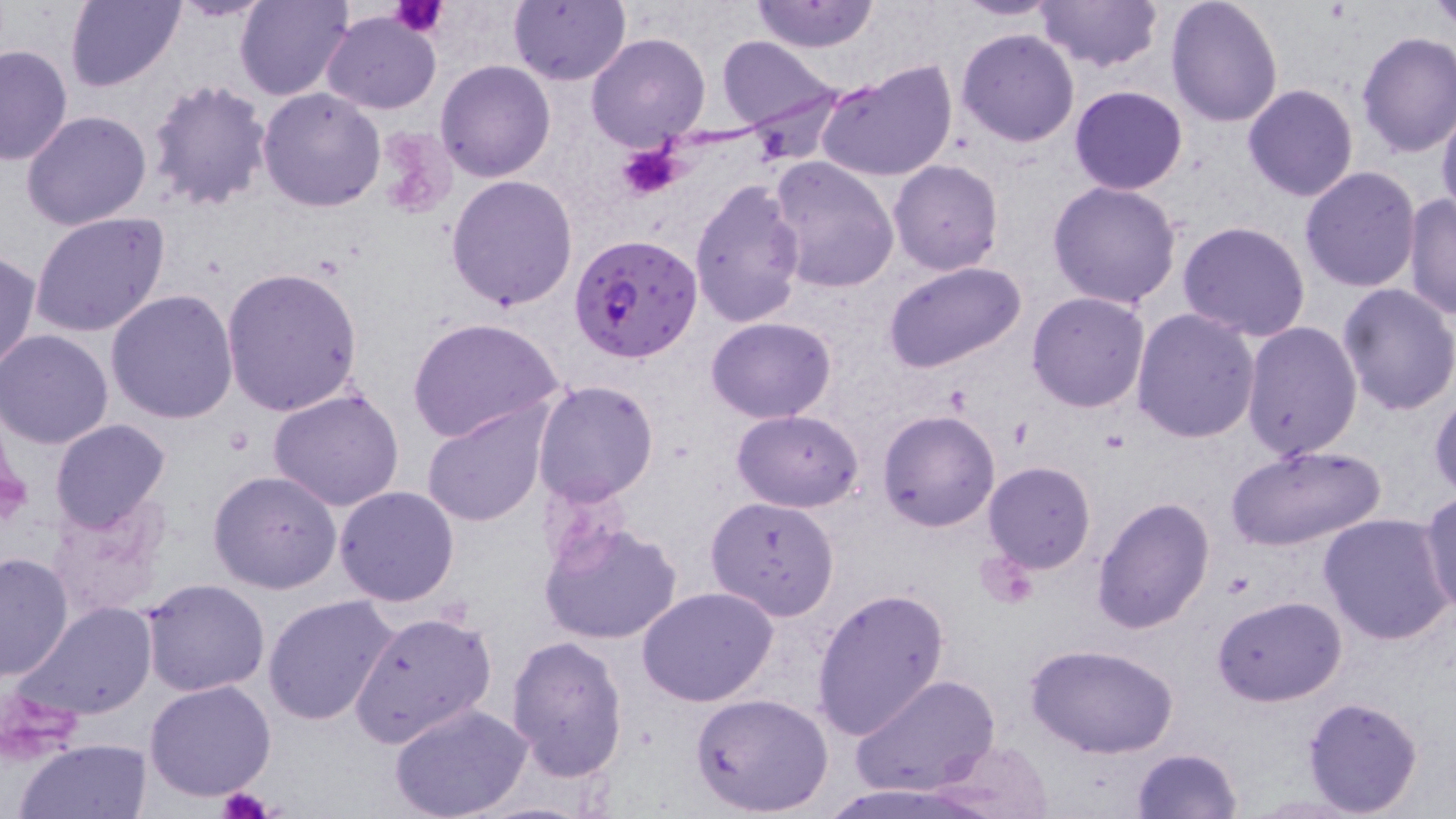

Approximate bounding boxes as (x1,y1)-(x2,y2) corner pairs in pixels. Plasmodium falciparum-infected red blood cell locations: (572,233)-(703,362). Platelet locations: (391,0)-(446,39), (615,144)-(685,201), (217,788)-(273,819). Uninfected red blood cell locations: (168,0)-(274,21), (235,0)-(353,102), (508,0)-(630,86), (750,0)-(880,54), (953,0)-(1060,21), (1035,0)-(1163,74), (1166,0)-(1284,126), (1428,0)-(1455,35), (64,1)-(185,90), (323,10)-(441,116), (956,28)-(1080,147), (1355,32)-(1456,158), (586,34)-(710,152), (716,36)-(835,131), (0,44)-(72,166), (435,60)-(555,183), (818,61)-(957,183), (146,79)-(272,213), (1243,83)-(1359,202), (1069,85)-(1188,195), (258,87)-(385,212), (1437,100)-(1456,226), (21,109)-(152,230), (766,155)-(899,292), (888,160)-(1004,275), (1299,167)-(1422,293), (446,175)-(579,311), (690,180)-(809,328), (1047,181)-(1182,310), (1402,194)-(1455,320), (30,211)-(170,338), (1177,220)-(1311,341), (0,250)-(41,373), (882,261)-(1026,375), (222,268)-(365,417), (1336,282)-(1456,417), (106,291)-(239,427), (1025,291)-(1151,412), (1132,308)-(1260,446), (706,316)-(837,422), (408,317)-(564,443), (1242,320)-(1363,460), (0,329)-(114,450), (532,378)-(659,505), (1429,385)-(1456,497), (265,387)-(407,513), (421,402)-(549,527), (732,409)-(864,513), (878,410)-(1000,531), (50,419)-(172,535), (1225,443)-(1387,552), (982,462)-(1096,573), (209,469)-(341,594), (333,485)-(458,607), (1420,493)-(1456,616), (706,496)-(840,621), (1091,496)-(1215,634), (47,498)-(170,622), (1319,514)-(1453,646), (540,520)-(684,646), (0,551)-(75,681), (141,577)-(271,696), (637,585)-(779,706), (810,587)-(949,739), (263,594)-(397,726), (1211,594)-(1347,706), (17,603)-(160,722), (349,608)-(498,748), (507,635)-(629,781), (1026,642)-(1179,759), (849,673)-(999,797), (144,680)-(277,802), (690,692)-(834,817), (1302,696)-(1425,816), (388,703)-(533,819), (14,736)-(153,819), (924,738)-(1055,816), (1130,747)-(1243,819). Slide-level diagnosis: Plasmodium falciparum. Single field of view. Optical microscopy. May-Grünwald-Giemsa-stained preparation. 1000x magnification. Thin blood smear. Image is 1456×819 pixels.